Assess this cell for malaria.
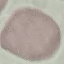

It is uninfected.

Thin smear of blood. Cell patch, automatically extracted from a larger field of view and resized to 64 × 64 pixels. Giemsa-stained preparation. Photographed with a smartphone camera at the microscope eyepiece.